Locate the red blood cells and classify each one as P. falciparum-infected, uninfected, or of indeterminate infection status.
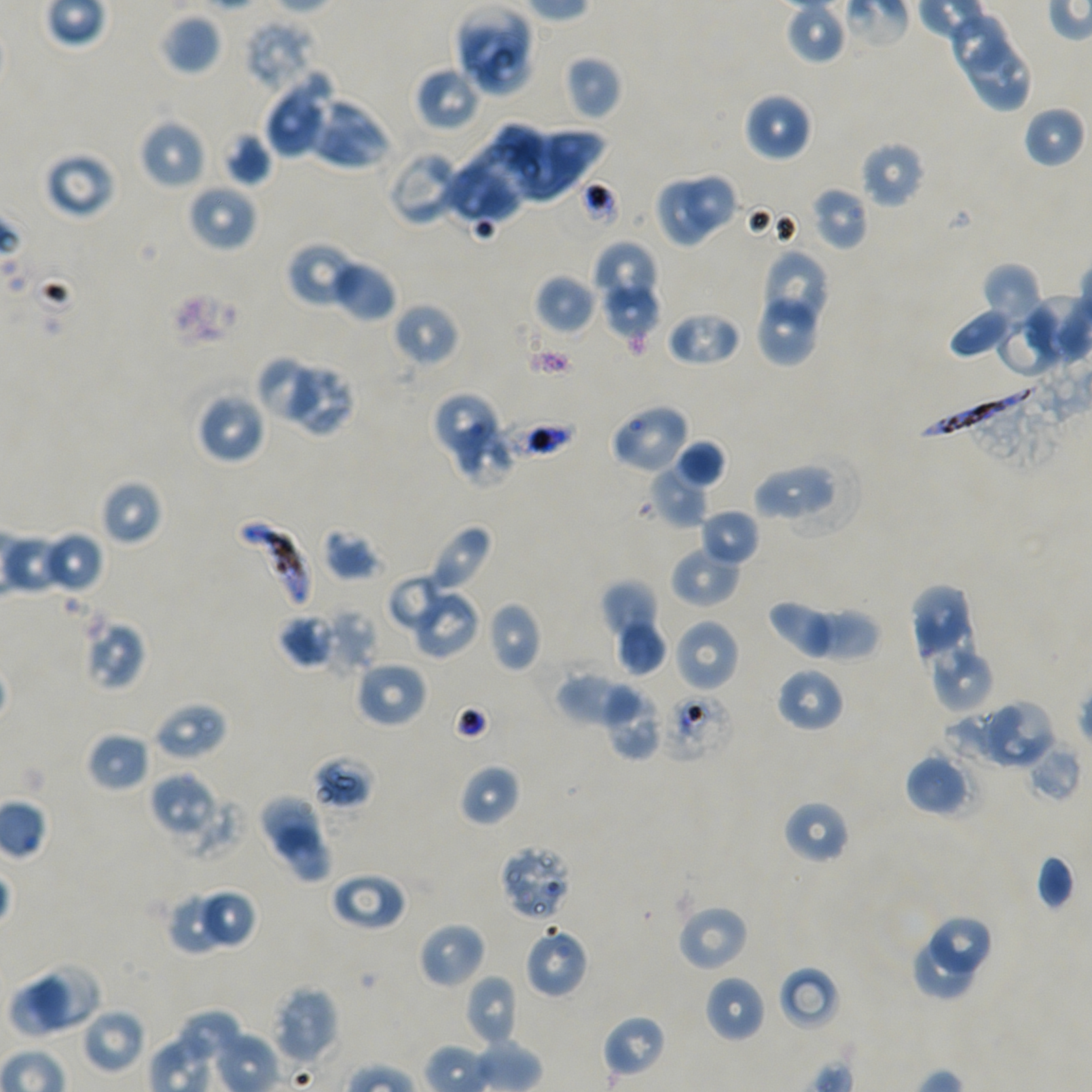

Approximate bounding boxes as {x1, y1, x2, y2} in pixels. Not every red blood cell is marked.
Infected red blood cells: {923, 378, 1049, 440}, {235, 520, 313, 611}.
Red blood cells of indeterminate infection status: {572, 180, 620, 232}, {494, 407, 582, 466}, {83, 619, 146, 690}, {662, 692, 735, 762}, {312, 756, 375, 810}, {499, 843, 575, 922}.
Uninfected red blood cells: {786, 1, 848, 65}, {455, 5, 532, 79}, {161, 14, 221, 75}, {953, 14, 1006, 74}, {244, 18, 318, 94}, {959, 40, 1035, 114}, {473, 44, 534, 99}, {564, 55, 621, 120}, {415, 66, 484, 132}, {263, 75, 333, 159}, {743, 92, 812, 162}, {305, 96, 392, 171}, {1023, 106, 1087, 169}, {483, 114, 551, 183}, {139, 118, 207, 190}, {509, 126, 603, 202}, {223, 130, 272, 185}, {860, 141, 925, 208}, {386, 145, 465, 225}, {444, 145, 526, 228}, {43, 150, 117, 219}, {680, 170, 740, 236}, {655, 176, 715, 248}, {187, 182, 258, 252}, {811, 186, 870, 250}, {287, 241, 361, 308}, {593, 241, 659, 309}, {759, 249, 831, 334}, {329, 257, 398, 322}, {981, 263, 1046, 331}, {534, 274, 597, 334}, {754, 279, 823, 367}, {601, 282, 660, 343}, {393, 302, 460, 367}, {948, 308, 1015, 359}, {665, 310, 741, 367}, {996, 316, 1063, 379}, {260, 357, 321, 421}, {291, 365, 357, 439}, {195, 391, 267, 465}, {431, 392, 499, 454}, {608, 403, 691, 474}, {454, 422, 515, 490}, {672, 439, 727, 490}, {754, 456, 836, 522}, {647, 464, 710, 528}, {100, 479, 162, 545}, {699, 508, 760, 568}, {426, 524, 493, 594}, {321, 528, 381, 581}, {40, 530, 105, 594}, {669, 544, 742, 608}, {388, 573, 448, 631}, {600, 581, 663, 663}, {909, 583, 968, 657}, {408, 589, 480, 660}, {767, 600, 844, 660}, {487, 602, 541, 672}, {802, 606, 879, 663}, {324, 608, 377, 674}, {278, 613, 336, 669}, {920, 616, 978, 682}, {614, 617, 668, 675}, {673, 618, 740, 693}, {934, 653, 995, 712}, {354, 659, 427, 729}, {776, 666, 845, 733}, {555, 670, 636, 728}, {601, 682, 663, 760}, {989, 699, 1057, 769}, {153, 702, 228, 761}, {945, 703, 1021, 765}, {86, 731, 151, 793}, {1023, 736, 1083, 803}, {905, 751, 972, 817}, {458, 763, 521, 826}, {149, 771, 216, 835}, {258, 795, 325, 861}, {783, 800, 850, 864}, {276, 828, 334, 883}, {1036, 852, 1076, 911}, {330, 871, 407, 931}, {200, 888, 259, 951}, {167, 895, 224, 956}, {676, 904, 750, 972}, {931, 914, 993, 977}, {418, 922, 486, 989}, {524, 926, 589, 999}, {913, 936, 977, 1001}, {29, 962, 102, 1030}, {778, 965, 841, 1032}, {464, 975, 520, 1049}, {704, 975, 766, 1043}, {10, 978, 73, 1040}, {272, 984, 340, 1066}, {80, 1006, 145, 1074}, {175, 1008, 244, 1063}, {603, 1015, 667, 1077}.

Giemsa-stained preparation. Thin blood film. P. falciparum strain NF54 in static in-vitro culture. Image is 1092×1092 pixels. Donor blood group A+/O+. Single field of view. Oil immersion, 100x objective (numerical aperture 1.45).